State which parasite is depicted.
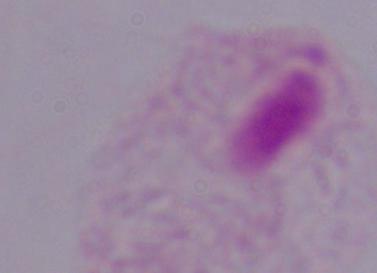

This is a trichomonad.

Summary:
  - Magnification: 1000x
  - Modality: photomicrograph